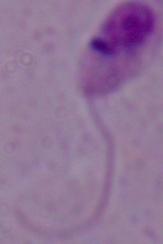

Summary:
  - Identification: Leishmania
  - Modality: photomicrograph
  - Magnification: 1000x